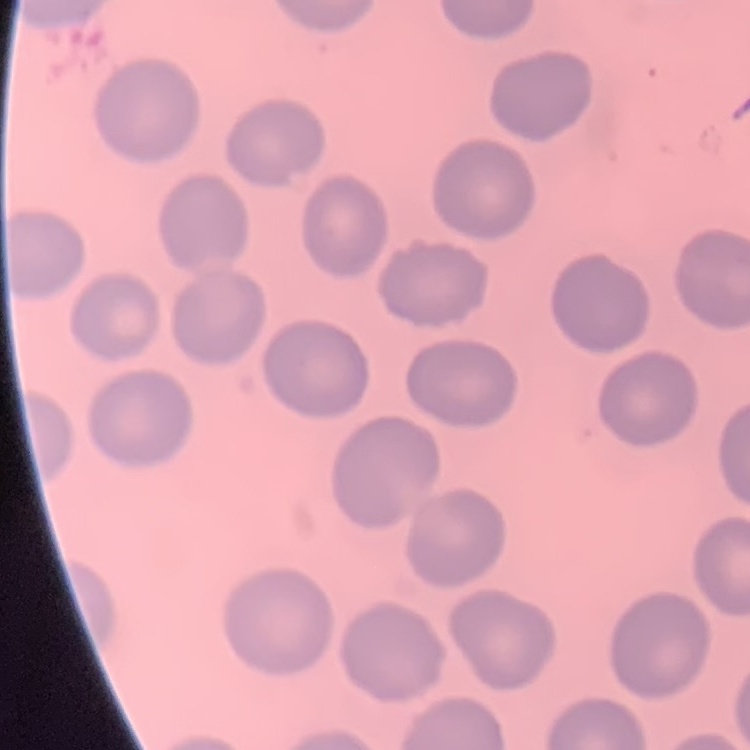
Summary:
  - Red blood cell morphology: no rouleaux formation
  - Image type: square crop of a larger photomicrograph
  - Preparation: thin blood film
  - Stain: Field's or Giemsa